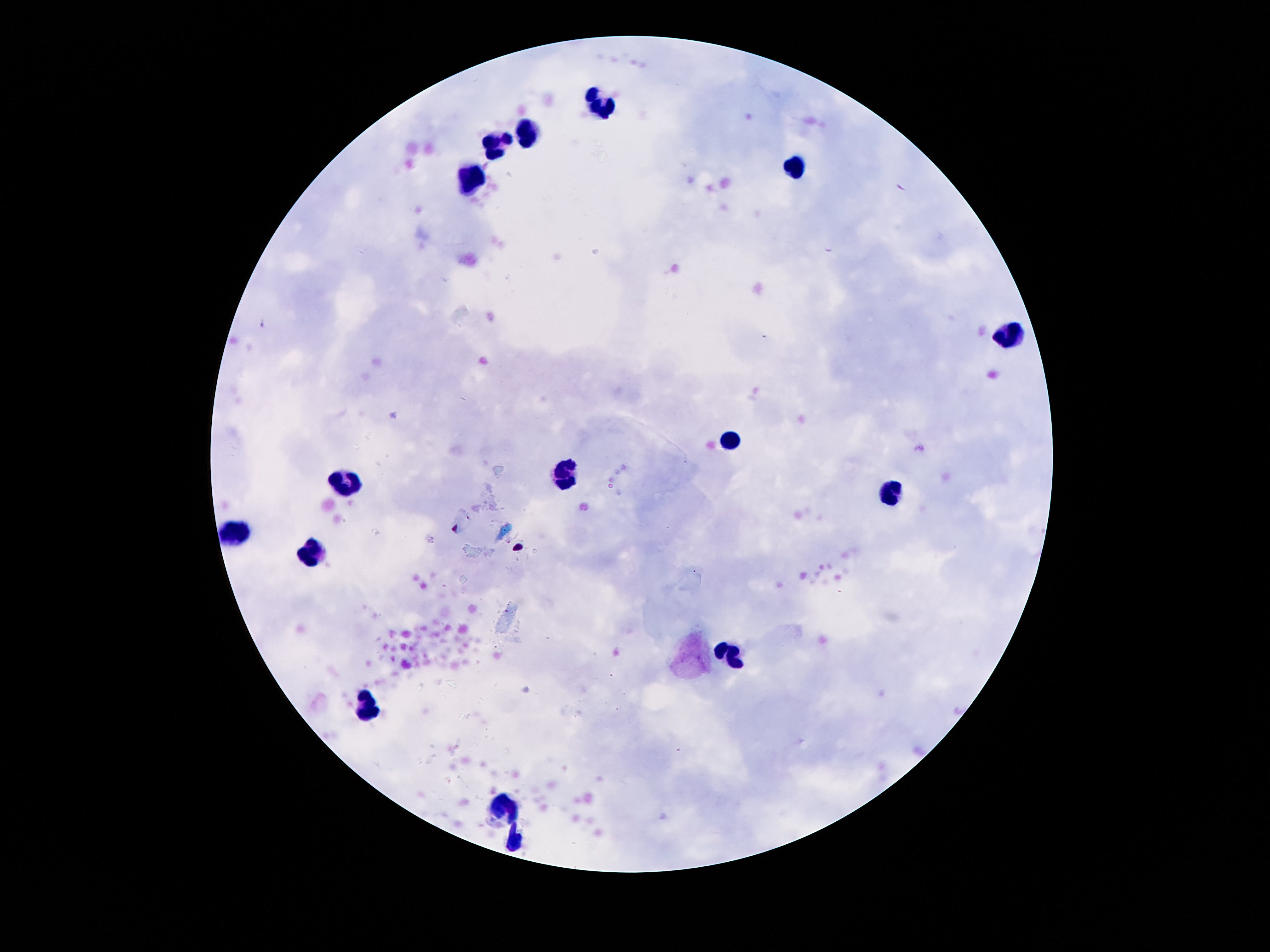 Approximate centers as [x, y] in pixels. Leukocyte locations: [599, 105], [526, 128], [496, 145], [793, 169], [470, 180], [1004, 332], [733, 441], [565, 475], [343, 486], [890, 494], [238, 531], [315, 550], [731, 656], [366, 706], [503, 807], [513, 840]. Giemsa-stained preparation. 100x magnification. Image is 1270×952 pixels. One field from this slide. Photographed through the microscope eyepiece with a smartphone camera. Thick blood film. Patient malaria status: uninfected.